Assess this cell for malaria.
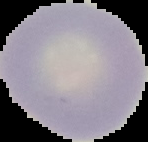

Uninfected.

From a thin blood film. Segmented cell region on a black background. Image is 148×142 pixels.